Name the blood parasite species.
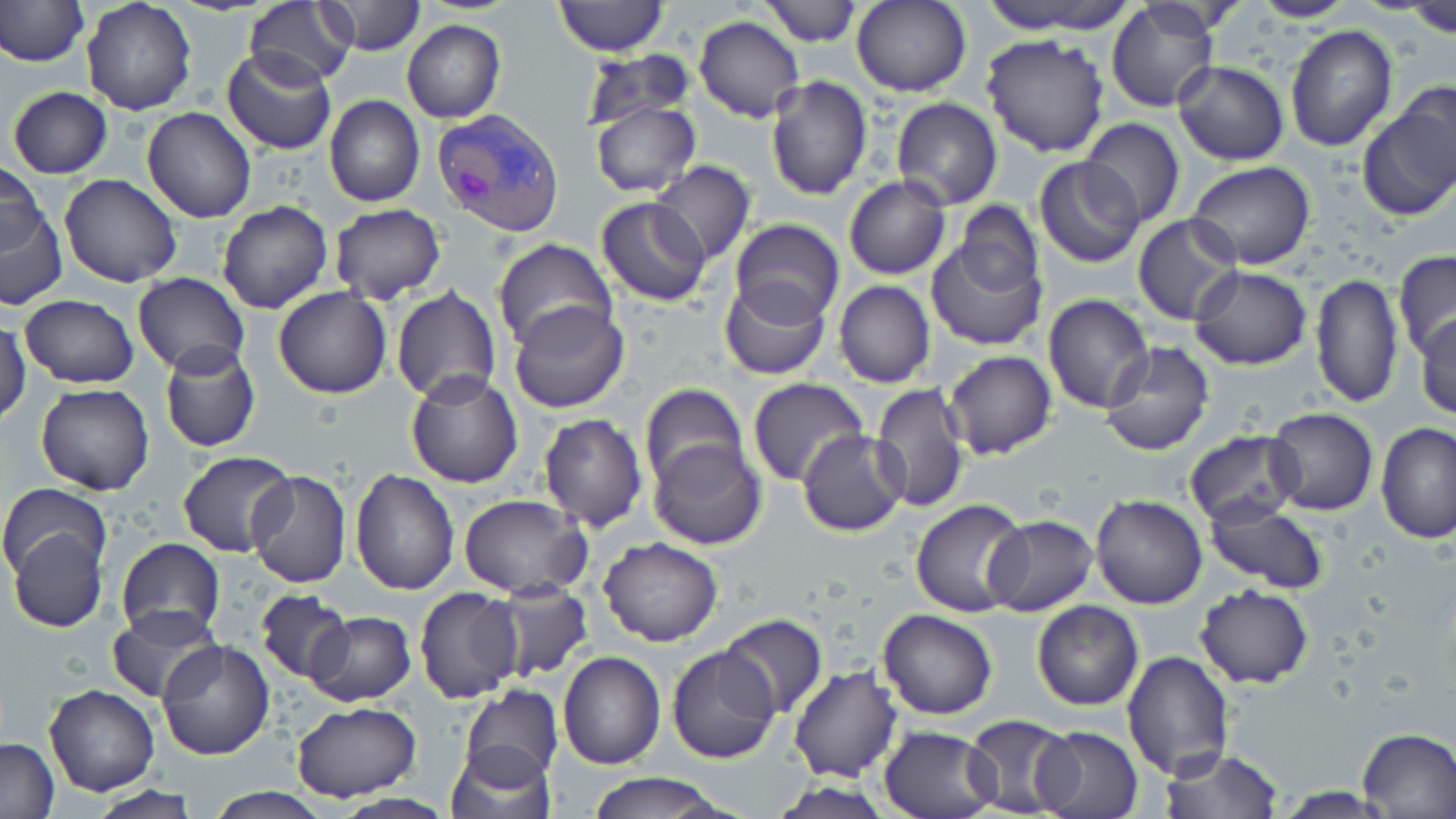

Plasmodium vivax.

Summary:
  - Coordinate format: approximate bounding boxes as (x1, y1, x2, y2) in pixels
  - Plasmodium vivax-infected red blood cell locations: (432, 109, 564, 236)
  - Uninfected red blood cell locations: (81, 0, 195, 116), (244, 0, 359, 90), (324, 0, 426, 56), (554, 0, 667, 57), (761, 0, 862, 47), (850, 0, 972, 97), (990, 0, 1143, 34), (1247, 0, 1358, 23), (0, 1, 87, 67), (1402, 2, 1456, 35), (1106, 3, 1220, 113), (693, 15, 805, 122), (403, 21, 505, 123), (1284, 26, 1398, 150), (981, 32, 1111, 157), (222, 47, 336, 156), (584, 49, 696, 129), (1173, 61, 1289, 165), (765, 76, 873, 202), (6, 86, 112, 178), (1357, 92, 1456, 221), (324, 96, 424, 207), (891, 97, 1003, 210), (589, 100, 701, 197), (142, 107, 256, 222), (1079, 118, 1184, 229), (1033, 156, 1145, 269), (1186, 160, 1314, 271), (1, 161, 49, 254), (648, 161, 755, 266), (59, 174, 182, 289), (843, 176, 951, 279), (595, 197, 710, 306), (0, 199, 68, 310), (217, 201, 334, 315), (954, 203, 1042, 298), (328, 204, 447, 306), (1133, 213, 1243, 325), (730, 218, 844, 324), (491, 238, 616, 351), (926, 238, 1048, 352), (1392, 250, 1456, 358), (1189, 265, 1312, 369), (133, 273, 249, 375), (1310, 275, 1402, 409), (718, 279, 831, 381), (834, 280, 934, 388), (273, 286, 393, 399), (391, 286, 502, 407), (1043, 294, 1153, 412), (19, 295, 139, 389), (508, 301, 630, 413), (1412, 314, 1456, 421), (0, 316, 30, 426), (159, 341, 260, 453), (1099, 342, 1215, 457), (943, 350, 1058, 460), (406, 370, 525, 489), (748, 378, 868, 488), (35, 383, 156, 495), (639, 383, 748, 493), (871, 383, 969, 515), (1264, 407, 1377, 516), (539, 412, 648, 532), (1377, 423, 1455, 545), (1183, 429, 1302, 528), (798, 430, 907, 534), (648, 439, 765, 550), (177, 451, 296, 559), (350, 467, 459, 594), (245, 470, 351, 588), (1, 482, 111, 581), (1090, 494, 1209, 610), (459, 495, 590, 600), (910, 498, 1030, 617), (1203, 498, 1330, 594), (982, 516, 1098, 616), (9, 526, 107, 633), (599, 536, 724, 646), (116, 538, 224, 641), (1195, 583, 1313, 688), (493, 584, 592, 681), (414, 586, 524, 705), (256, 590, 354, 683), (1031, 600, 1144, 710), (107, 606, 223, 704), (878, 608, 997, 720), (304, 612, 414, 707), (718, 615, 828, 718), (155, 640, 275, 759), (665, 643, 782, 765), (1121, 650, 1235, 779), (557, 651, 665, 768), (789, 666, 902, 782), (45, 685, 159, 797), (460, 685, 563, 786), (290, 701, 422, 800), (963, 713, 1076, 816), (878, 723, 1001, 818), (1032, 726, 1142, 819), (1357, 728, 1456, 816), (1, 737, 59, 817), (445, 743, 555, 819), (1159, 746, 1283, 818), (582, 772, 734, 818), (200, 786, 339, 818)
  - Stain: May-Grünwald-Giemsa
  - Preparation: thin blood film
  - Modality: light microscopy
  - Image size: 1456×819 pixels
  - Magnification: 1000x
  - Field of view: one of a larger specimen